Outline each blood parasite and name the species.
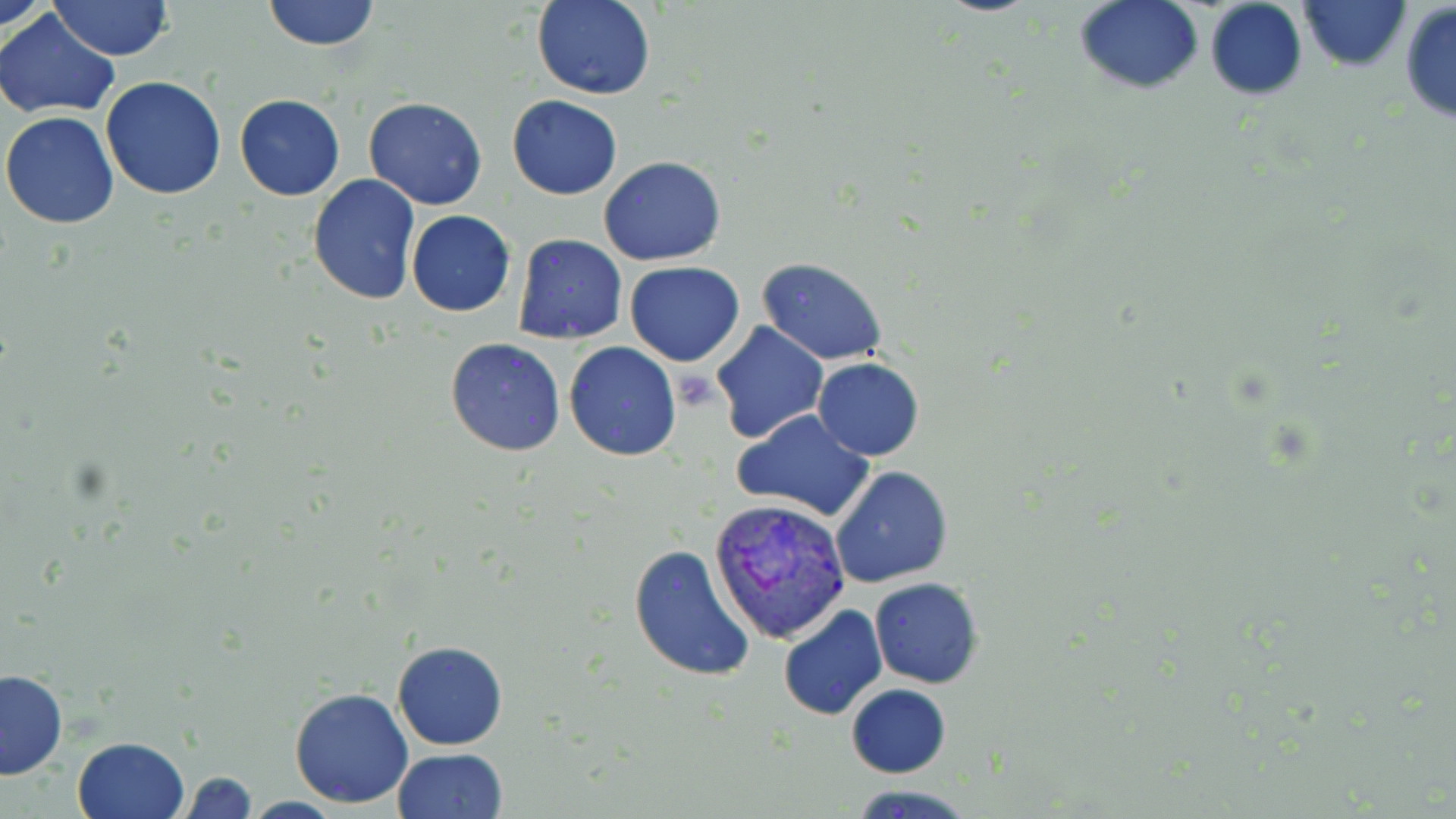
Approximate bounding boxes as [x1, y1, x2, y2] in pixels.
Plasmodium vivax-infected red blood cells: [709, 496, 849, 645].
No Plasmodium falciparum, Plasmodium ovale, Plasmodium malariae, Babesia divergens, or Trypanosoma brucei observed.

Uninfected red blood cell locations: [49, 0, 174, 61], [263, 0, 380, 51], [1075, 0, 1204, 93], [1298, 0, 1411, 74], [533, 1, 654, 100], [1204, 1, 1308, 100], [1398, 4, 1455, 125], [1, 10, 120, 117], [100, 75, 226, 200], [234, 95, 345, 201], [506, 95, 622, 200], [364, 97, 486, 210], [1, 111, 121, 228], [599, 156, 727, 266], [307, 174, 420, 305], [406, 210, 516, 317], [512, 234, 626, 344], [758, 258, 887, 365], [625, 262, 745, 366], [711, 321, 829, 444], [445, 338, 565, 457], [564, 341, 681, 461], [813, 357, 925, 460], [733, 409, 876, 523], [830, 465, 952, 587], [627, 544, 756, 683], [869, 577, 983, 687], [778, 606, 887, 720], [392, 640, 508, 750], [0, 669, 68, 780], [846, 684, 950, 778], [289, 686, 415, 809], [72, 736, 188, 818], [392, 747, 508, 819], [176, 770, 259, 819], [847, 783, 978, 819]. Platelet locations: [673, 369, 715, 409]. Slide-level diagnosis: Plasmodium vivax. May-Grünwald-Giemsa stain. Image is 1456×819 pixels. Thin blood film. Optical microscopy. One field of a larger specimen. 1000x magnification.